State which parasite is depicted.
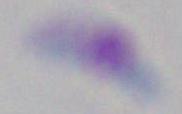

This is Toxoplasma gondii.

1000x magnification. Micrograph.